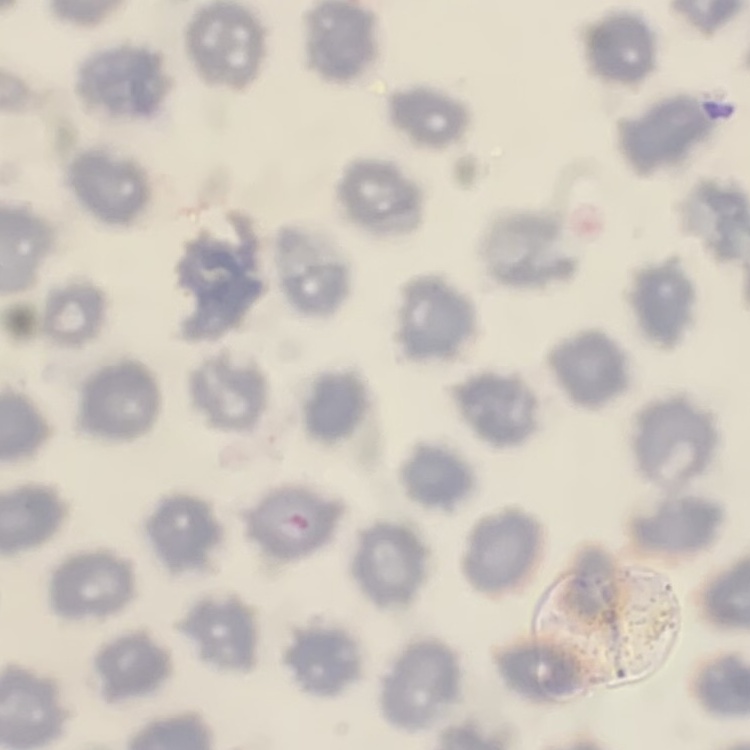

The erythrocytes exhibit no rouleaux formation. Stained with either Field's or Giemsa. One tile cut from a larger photomicrograph. Thin peripheral smear.